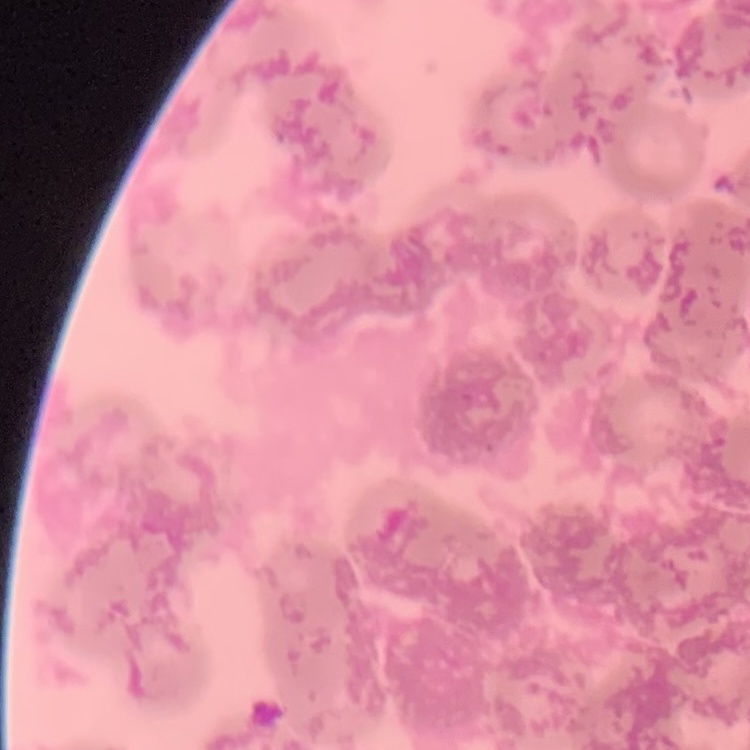
erythrocyte morphology = rouleaux formation
stain = Field's or Giemsa
preparation = thin blood film
image type = square crop of a larger photomicrograph